Report the malaria status of this cell.
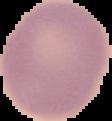
It is uninfected.

From a thin blood smear. Image is 112×121 pixels. Segmented cell region on a black background.